Classify this cell by malaria status.
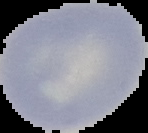

Uninfected.

Summary:
  - Image type: cell region segmented out of the field of view; surrounding area masked to black
  - Preparation: thin blood smear
  - Image size: 148×133 pixels